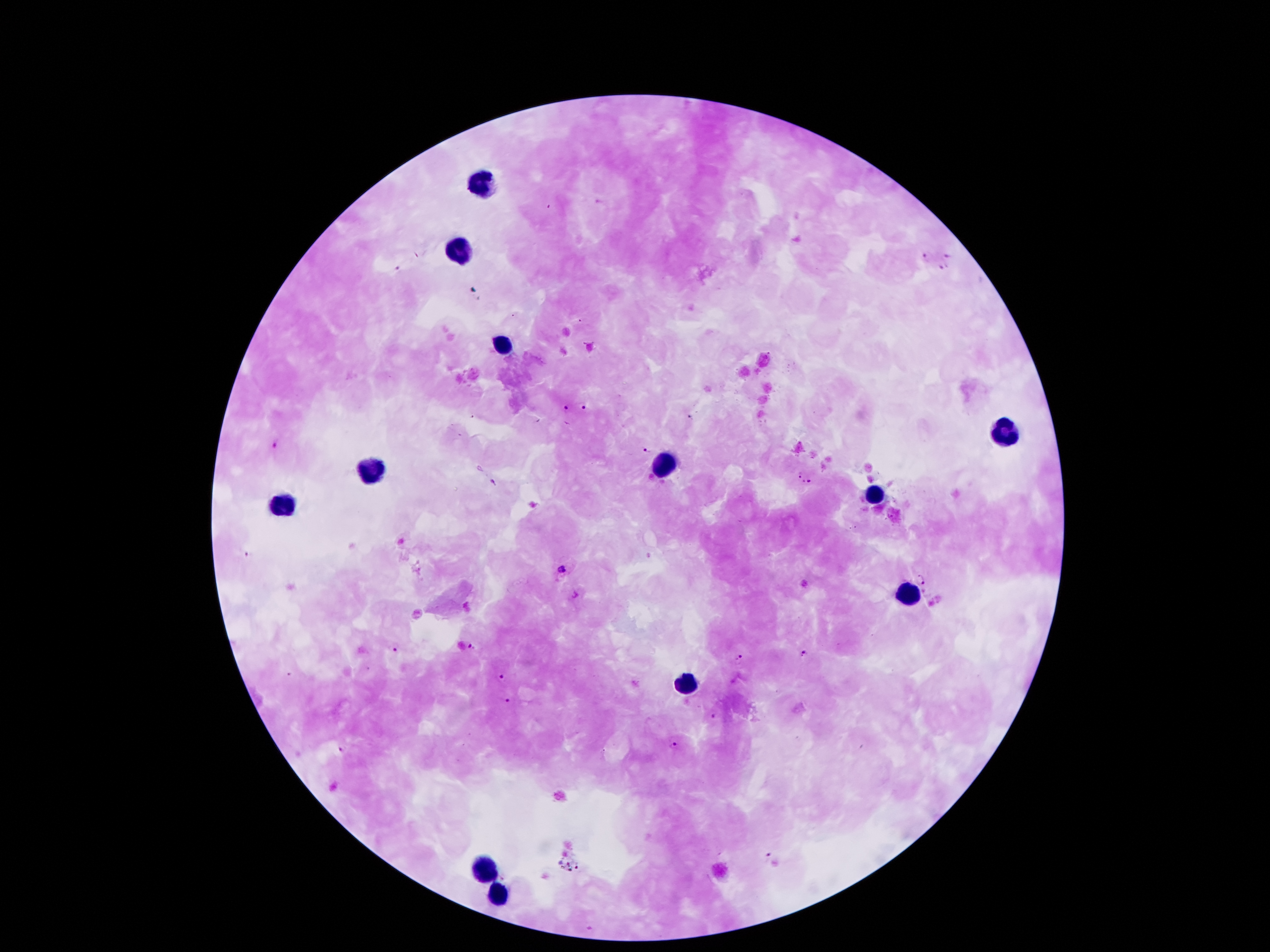
Approximate centers as (x, y) in pixels.
Summary:
  - Malaria parasite locations: (946, 255), (925, 258), (943, 267), (564, 408), (587, 408), (689, 417), (277, 444), (647, 450), (798, 473), (812, 481), (248, 551), (561, 570), (922, 579), (471, 646), (396, 649), (804, 655), (740, 657), (502, 675), (508, 701), (712, 716), (344, 745), (673, 748), (767, 855), (590, 929)
  - Leukocyte locations: (485, 185), (459, 251), (502, 345), (1004, 429), (666, 466), (371, 470), (877, 495), (281, 503), (910, 593), (690, 683), (483, 870), (496, 894)
  - Field of view: single
  - Image size: 1270×952 pixels
  - Capture: smartphone through the microscope eyepiece
  - Patient malaria status: positive for Plasmodium falciparum
  - Preparation: thick blood film
  - Stain: Giemsa
  - Magnification: 100x